Identify the parasite.
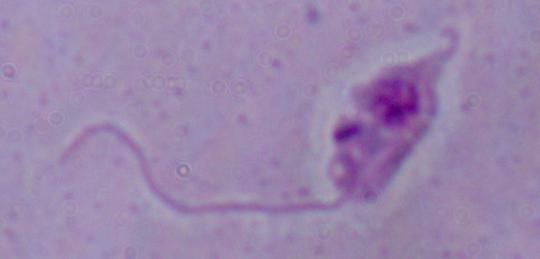

Leishmania.

Captured at 1000x magnification. Micrograph.